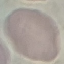

{
  "result": "no malaria parasites seen",
  "capture": "smartphone through the microscope eyepiece",
  "image_type": "cell patch, automatically extracted from a larger field of view and resized to 64 × 64 pixels",
  "stain": "Giemsa",
  "preparation": "thin smear"
}